Assess the morphology of the erythrocytes.
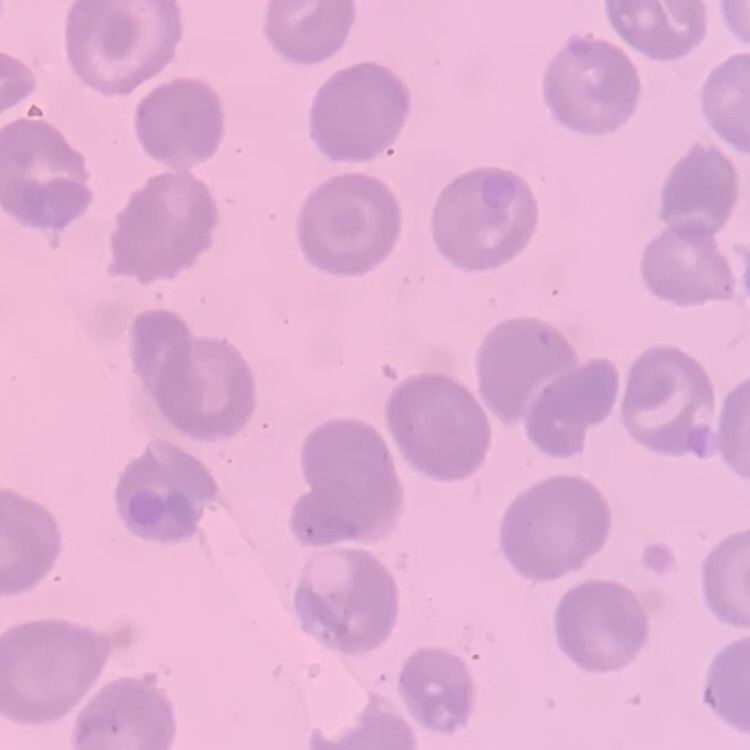
They show no rouleaux formation.

Summary:
  - Image type: one tile cut from a larger photomicrograph
  - Stain: Field's or Giemsa
  - Preparation: thin blood film